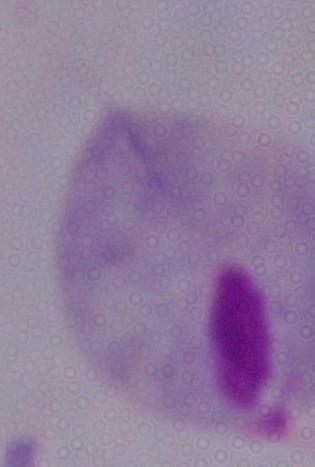
Summary:
  - Magnification: 1000x
  - Identification: trichomonad
  - Modality: micrograph